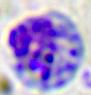
magnification = 400x
identification = white blood cell
modality = micrograph